Give the position of every Plasmodium falciparum parasite, noting its life-cycle stage.
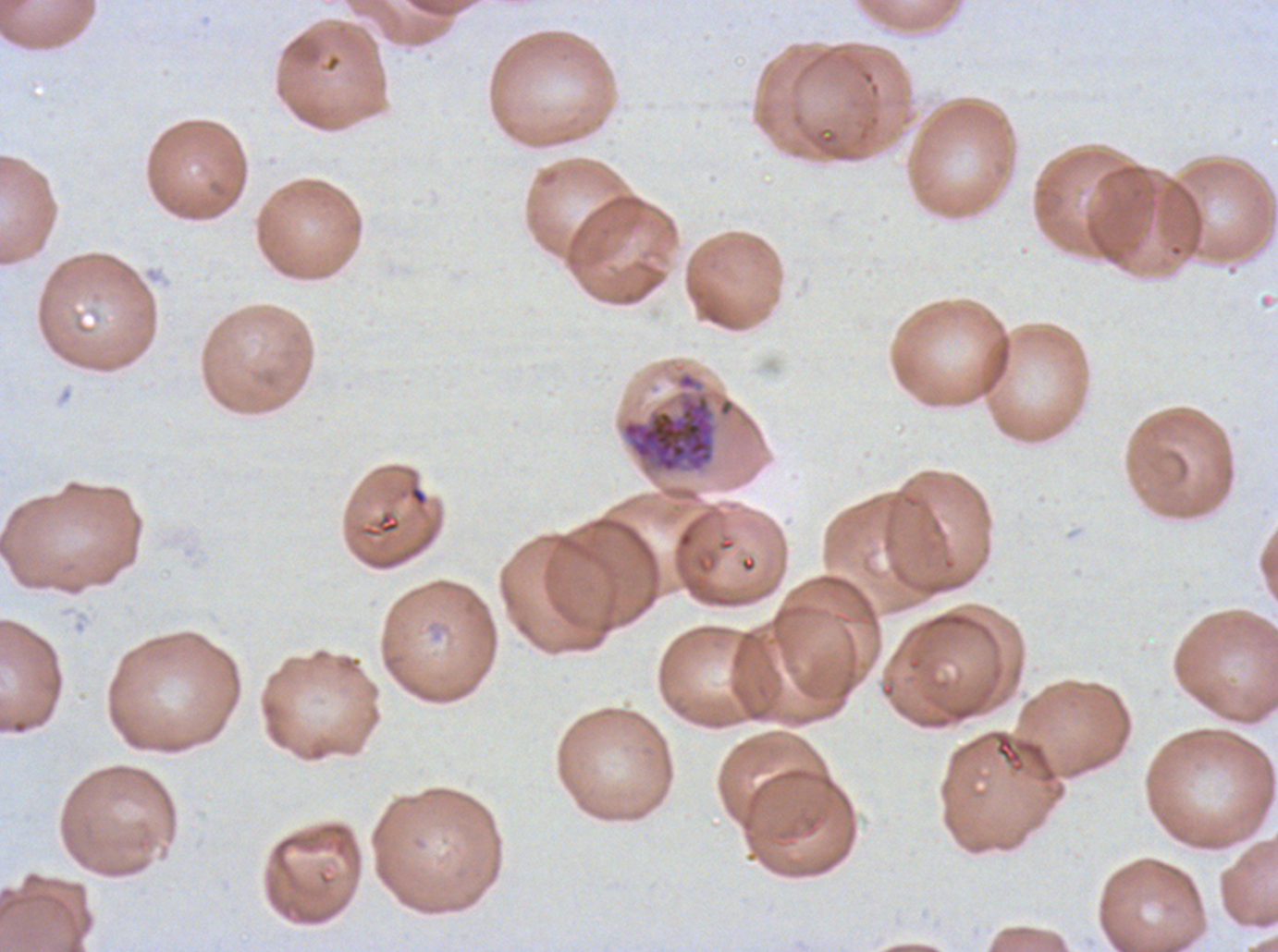
Approximate bounding rectangles given as corner coordinates in pixels from the top-left.
Late schizonts: (x1=620, y1=371, x2=719, y2=475).
No rings, late-ring/early-trophozoite forms, mid trophozoites, late trophozoites, early schizonts, segmenters, or gametocytes observed.

Image is 1278×952 pixels. Plasmodium falciparum from a patient in The Gambia, cultured ex vivo for 24 to 48 hours. One sub-image of a larger composite. Thin blood smear. Giemsa-stained preparation.